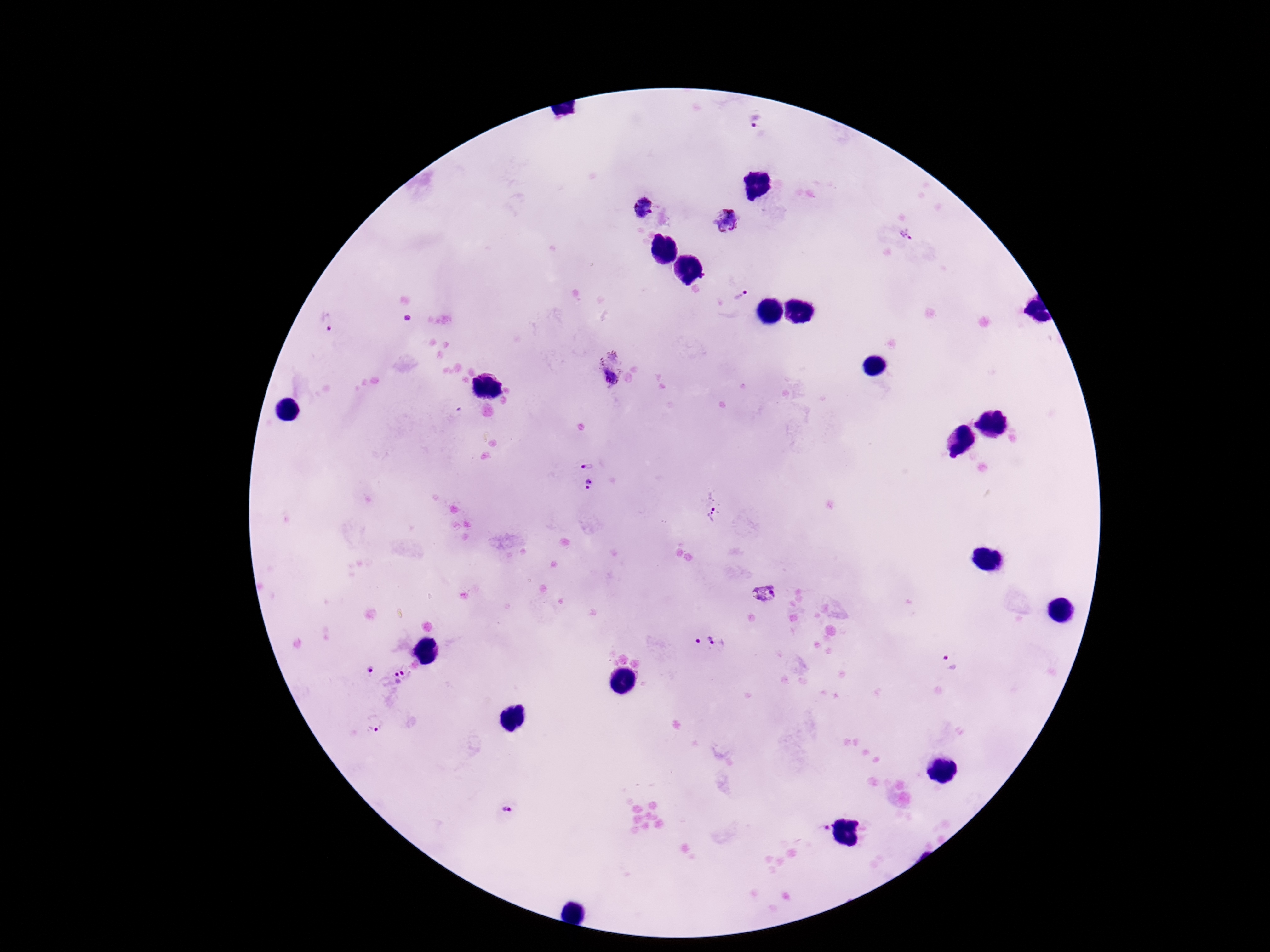
Approximate centers as [x, y] in pixels. Plasmodium parasite locations: [755, 123], [643, 208], [727, 220], [907, 236], [706, 278], [740, 294], [325, 320], [611, 369], [589, 466], [590, 487], [711, 510], [765, 594], [710, 643], [950, 664], [366, 671], [396, 684], [374, 723], [505, 811], [823, 829]. Giemsa-stained preparation. Single field of view. Thick blood smear. Image is 1270×952 pixels. Patient malaria status: positive. 100x magnification. Smartphone photograph taken through the microscope eyepiece.